Name the cell type shown.
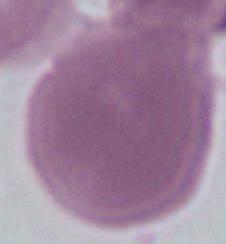
This is an erythrocyte.

{
  "modality": "photomicrograph",
  "magnification": "1000x"
}